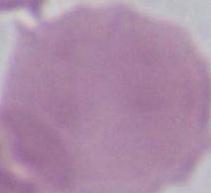
A red blood cell is shown. 1000x magnification. Micrograph.